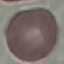
Result: no malaria parasites detected. Photographed with a smartphone camera at the microscope eyepiece. Cell patch, automatically extracted from a larger field of view and resized to 64 × 64 pixels. Thin blood smear. Giemsa-stained preparation.